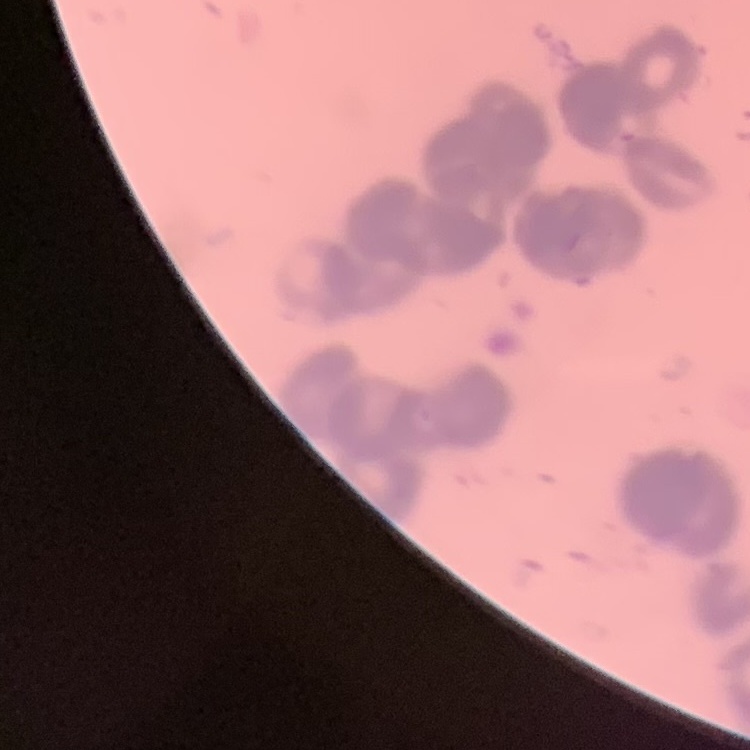
Summary:
  - Erythrocyte morphology: rouleaux formation
  - Image type: square crop of a larger photomicrograph
  - Stain: Field's or Giemsa
  - Preparation: thin blood film